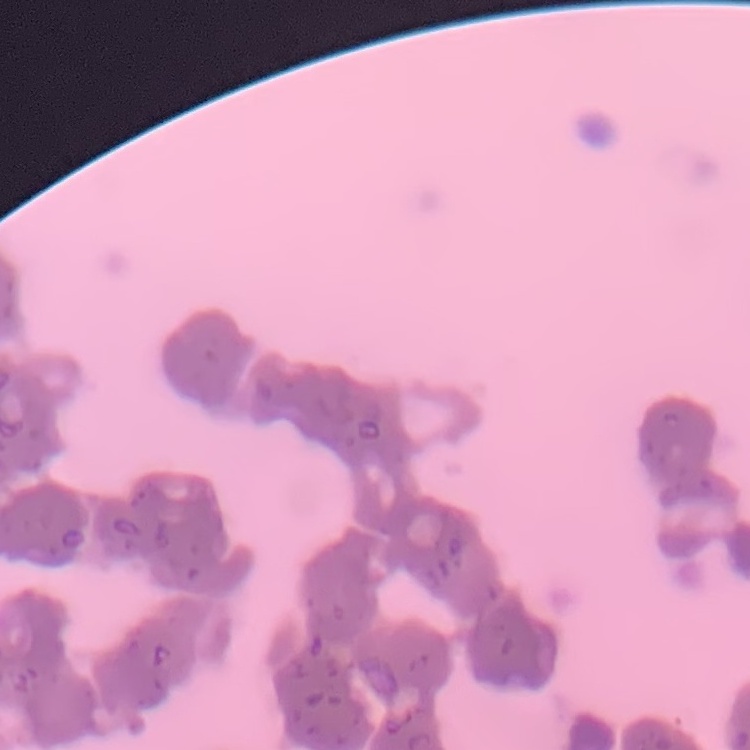

The red blood cells show rouleaux formation. Field's or Giemsa stain. Thin peripheral smear. Square crop of a larger photomicrograph.